Report the malaria status of this cell.
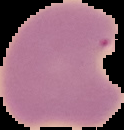
It is parasitized.

image_type: segmented cell region with the area outside set to black
preparation: thin blood smear
image_size: 124×130 pixels